Identify the cell.
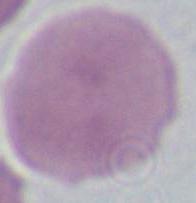
An erythrocyte.

Summary:
  - Modality: micrograph
  - Magnification: 1000x